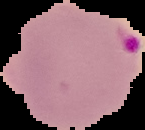
preparation: thin blood film
malaria_status: parasitized
image_size: 145×130 pixels
image_type: cell region segmented out of the field of view; surrounding area masked to black